Report the malaria status of this cell.
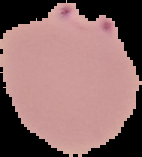

It is parasitized.

{
  "image_size": "142×157 pixels",
  "image_type": "cell region segmented out of the field of view; surrounding area masked to black",
  "preparation": "thin blood film"
}